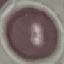
Summary:
  - Result: negative for malaria parasites
  - Preparation: thin blood smear
  - Capture: smartphone through the microscope eyepiece
  - Stain: Giemsa
  - Image type: cell patch, automatically extracted from a larger field of view and resized to 64 × 64 pixels